Assess the morphology of the erythrocytes.
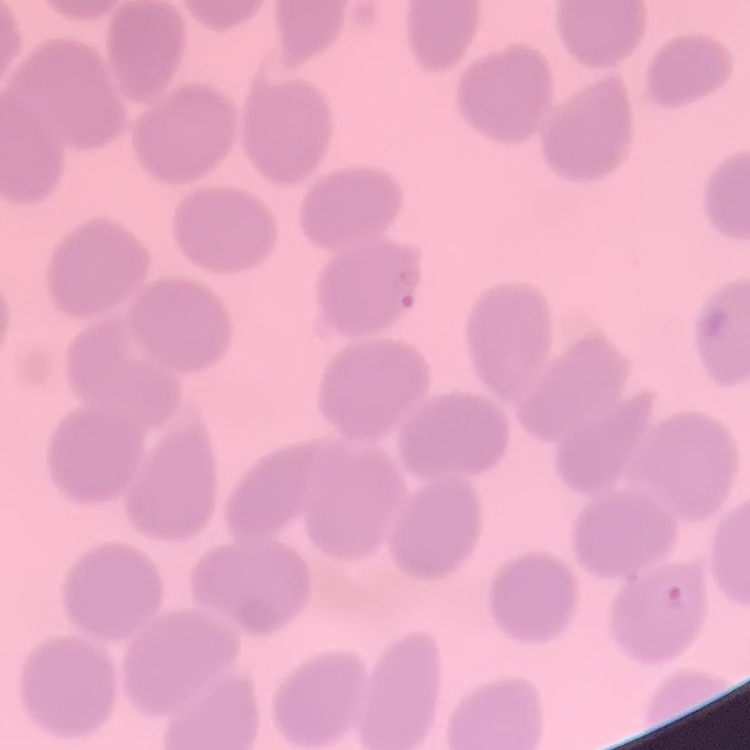

They show no rouleaux formation.

Square crop of a larger photomicrograph. Thin peripheral smear. Stained with either Field's or Giemsa.